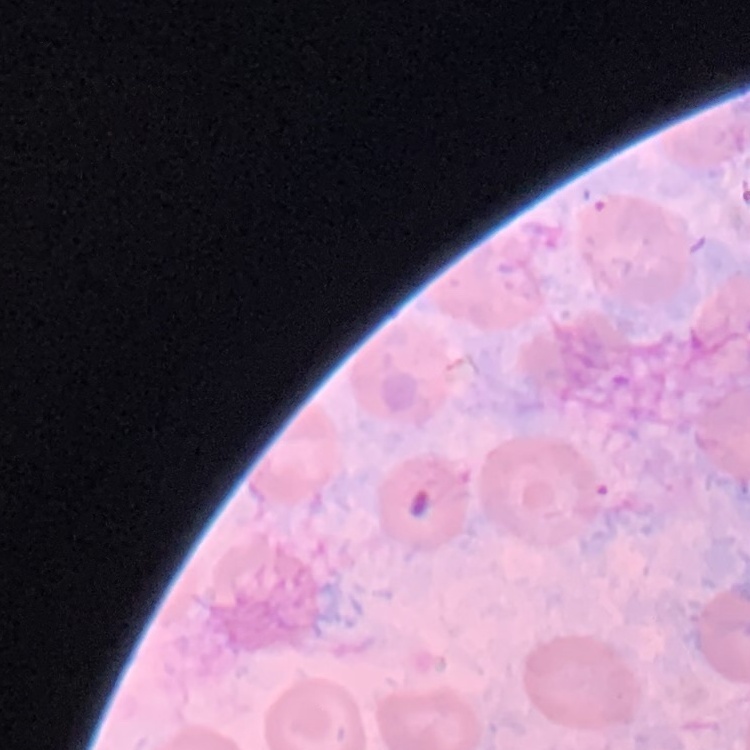

{
  "erythrocyte_morphology": "no rouleaux formation",
  "preparation": "thin peripheral smear",
  "stain": "Field's or Giemsa",
  "image_type": "one tile cut from a larger photomicrograph"
}